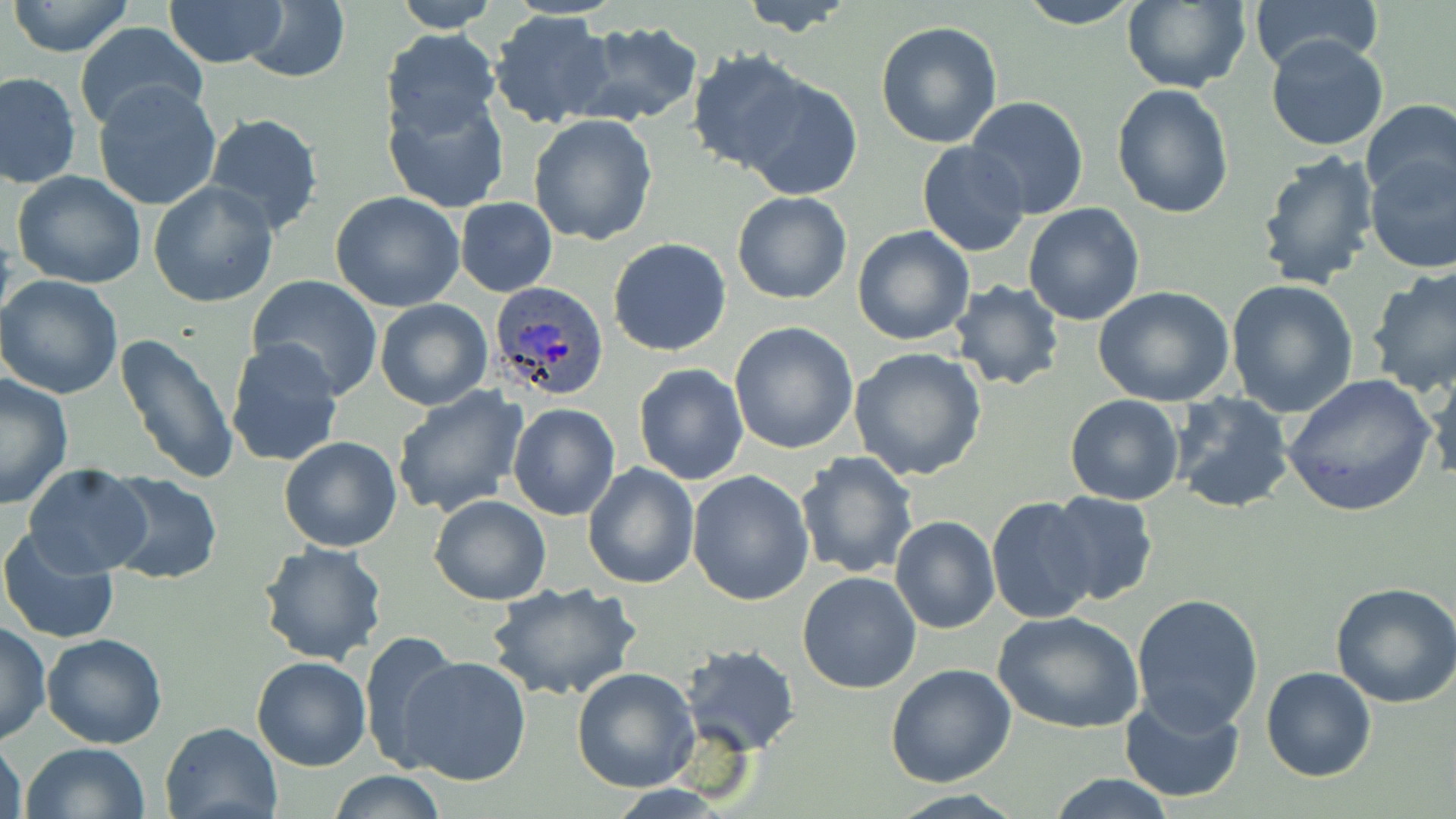
slide-level diagnosis = Plasmodium ovale
modality = optical microscopy
Plasmodium ovale-infected red blood cell locations = approximate bounding boxes as [x1, y1, x2, y2] in pixels: [490, 281, 612, 402]
field of view = one of a larger specimen
stain = May-Grünwald-Giemsa
image size = 1456×819 pixels
uninfected red blood cell locations = approximate bounding boxes as [x1, y1, x2, y2] in pixels: [163, 0, 289, 70], [389, 0, 499, 32], [737, 0, 861, 36], [1014, 0, 1144, 28], [1248, 0, 1383, 74], [7, 1, 134, 56], [243, 1, 349, 83], [1119, 1, 1251, 92], [488, 9, 615, 130], [571, 20, 705, 128], [875, 21, 1004, 149], [73, 22, 208, 135], [381, 27, 501, 136], [1265, 34, 1389, 151], [684, 50, 814, 174], [1, 72, 80, 189], [740, 75, 863, 198], [93, 81, 221, 211], [1111, 83, 1235, 218], [384, 90, 509, 214], [965, 96, 1091, 220], [1359, 100, 1456, 204], [201, 112, 325, 237], [528, 113, 658, 246], [917, 141, 1029, 256], [1256, 148, 1383, 292], [1363, 155, 1456, 272], [11, 171, 149, 292], [149, 180, 278, 306], [331, 192, 466, 312], [732, 192, 853, 305], [456, 198, 557, 295], [1023, 202, 1145, 325], [852, 225, 976, 346], [608, 238, 731, 356], [1367, 266, 1456, 397], [0, 274, 124, 400], [246, 275, 384, 397], [1226, 278, 1359, 415], [949, 280, 1064, 391], [1094, 286, 1237, 407], [373, 298, 493, 410], [729, 321, 859, 453], [113, 332, 241, 485], [224, 338, 346, 470], [847, 347, 989, 482], [1425, 356, 1456, 486], [633, 363, 748, 485], [0, 372, 76, 508], [1281, 373, 1436, 518], [390, 386, 528, 518], [1170, 393, 1294, 514], [1064, 394, 1185, 506], [507, 401, 621, 522], [278, 436, 402, 552], [794, 453, 918, 579], [583, 462, 701, 589], [23, 464, 152, 577], [687, 471, 815, 607], [103, 473, 224, 586], [1045, 491, 1157, 606], [429, 494, 552, 606], [987, 497, 1098, 623], [890, 515, 999, 634], [0, 526, 121, 646], [255, 542, 389, 666], [797, 570, 924, 694], [487, 580, 642, 703], [1331, 580, 1456, 707], [1131, 592, 1263, 734], [993, 610, 1144, 734], [0, 622, 51, 747], [357, 632, 460, 773], [41, 634, 167, 749], [679, 643, 801, 754], [251, 656, 374, 771], [398, 657, 532, 787], [885, 664, 1016, 788], [571, 667, 700, 792], [1262, 667, 1376, 782], [1119, 693, 1247, 804], [160, 720, 284, 819], [0, 735, 26, 819], [21, 743, 149, 819], [326, 771, 448, 817], [1043, 773, 1181, 818], [882, 790, 1029, 819]
magnification = 1000x
preparation = thin blood film